Mark where platelets are.
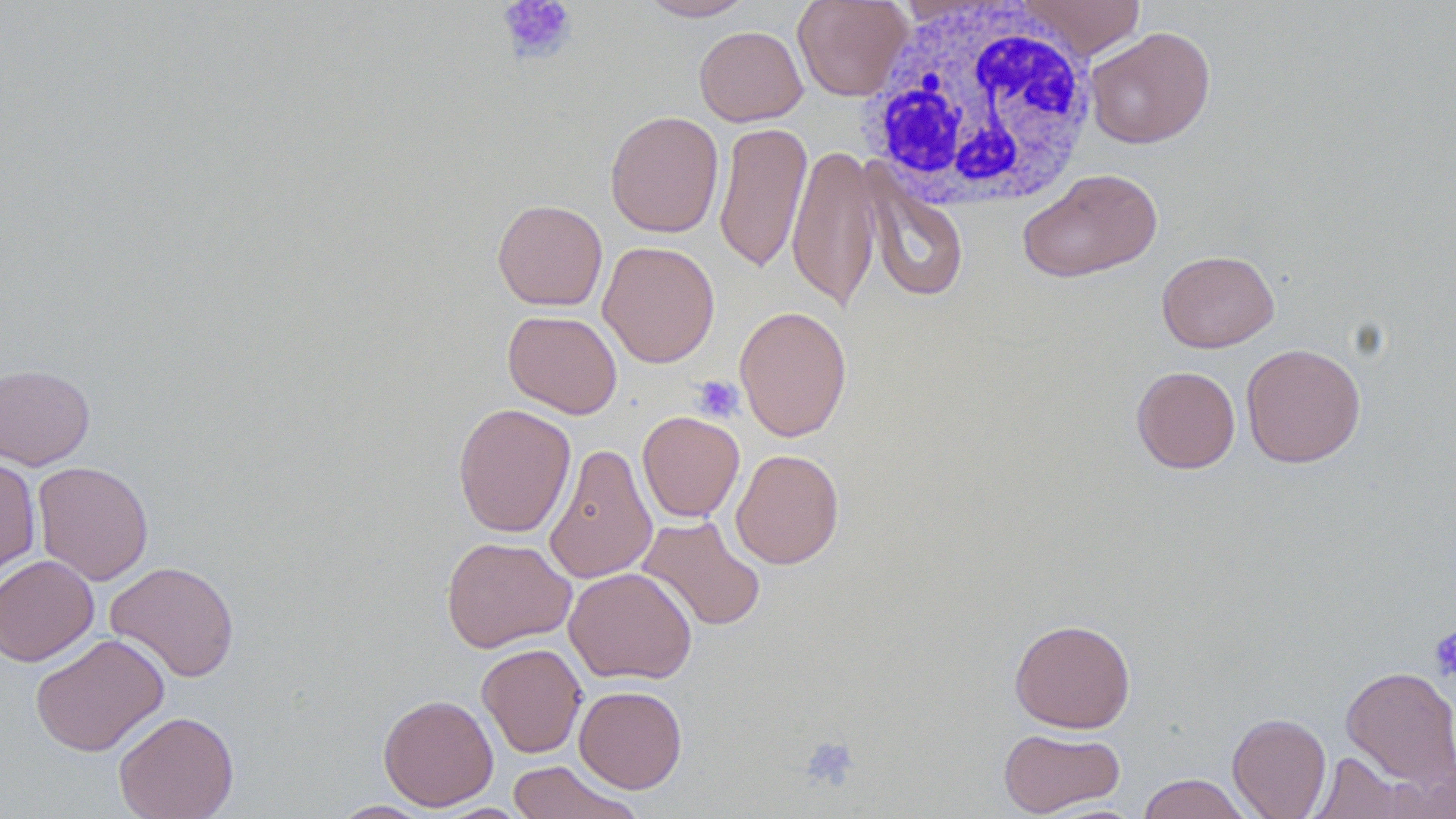

Approximate bounding boxes as named x1/y1/x2/y2 corners in pixels.
Platelets: (x1=497, y1=0, x2=578, y2=64), (x1=692, y1=375, x2=744, y2=423), (x1=1429, y1=626, x2=1456, y2=682), (x1=799, y1=735, x2=860, y2=791).

Summary:
  - Uninfected red blood cell locations: (x1=637, y1=0, x2=759, y2=21), (x1=792, y1=0, x2=912, y2=101), (x1=1016, y1=0, x2=1147, y2=59), (x1=694, y1=25, x2=807, y2=126), (x1=1084, y1=26, x2=1216, y2=149), (x1=605, y1=110, x2=724, y2=238), (x1=713, y1=120, x2=812, y2=273), (x1=787, y1=143, x2=881, y2=313), (x1=860, y1=165, x2=969, y2=304), (x1=1017, y1=167, x2=1163, y2=283), (x1=492, y1=198, x2=608, y2=311), (x1=598, y1=240, x2=720, y2=368), (x1=1157, y1=249, x2=1279, y2=353), (x1=734, y1=305, x2=852, y2=442), (x1=503, y1=310, x2=622, y2=419), (x1=1241, y1=343, x2=1366, y2=468), (x1=0, y1=363, x2=95, y2=470), (x1=1131, y1=366, x2=1241, y2=473), (x1=452, y1=403, x2=576, y2=537), (x1=637, y1=411, x2=745, y2=522), (x1=543, y1=443, x2=658, y2=584), (x1=731, y1=449, x2=844, y2=569), (x1=0, y1=456, x2=41, y2=581), (x1=32, y1=460, x2=154, y2=586), (x1=636, y1=515, x2=766, y2=632), (x1=440, y1=536, x2=576, y2=653), (x1=0, y1=554, x2=100, y2=666), (x1=105, y1=560, x2=240, y2=682), (x1=564, y1=567, x2=697, y2=684), (x1=1009, y1=618, x2=1135, y2=733), (x1=30, y1=632, x2=169, y2=756), (x1=476, y1=643, x2=587, y2=758), (x1=1340, y1=665, x2=1456, y2=789), (x1=573, y1=685, x2=687, y2=793), (x1=378, y1=693, x2=499, y2=811), (x1=113, y1=710, x2=239, y2=819), (x1=1227, y1=712, x2=1331, y2=819), (x1=997, y1=727, x2=1125, y2=817), (x1=1308, y1=751, x2=1414, y2=818), (x1=506, y1=760, x2=644, y2=819), (x1=1137, y1=773, x2=1254, y2=819), (x1=328, y1=800, x2=435, y2=818)
  - White blood cell locations: (x1=864, y1=1, x2=1099, y2=212)
  - Slide-level diagnosis: no evidence of blood parasites
  - Stain: May-Grünwald-Giemsa
  - Preparation: thin blood film
  - Field of view: single
  - Modality: optical microscopy
  - Image size: 1456×819 pixels
  - Magnification: 1000x